Outline each P. falciparum parasite and classify it by life-cycle stage.
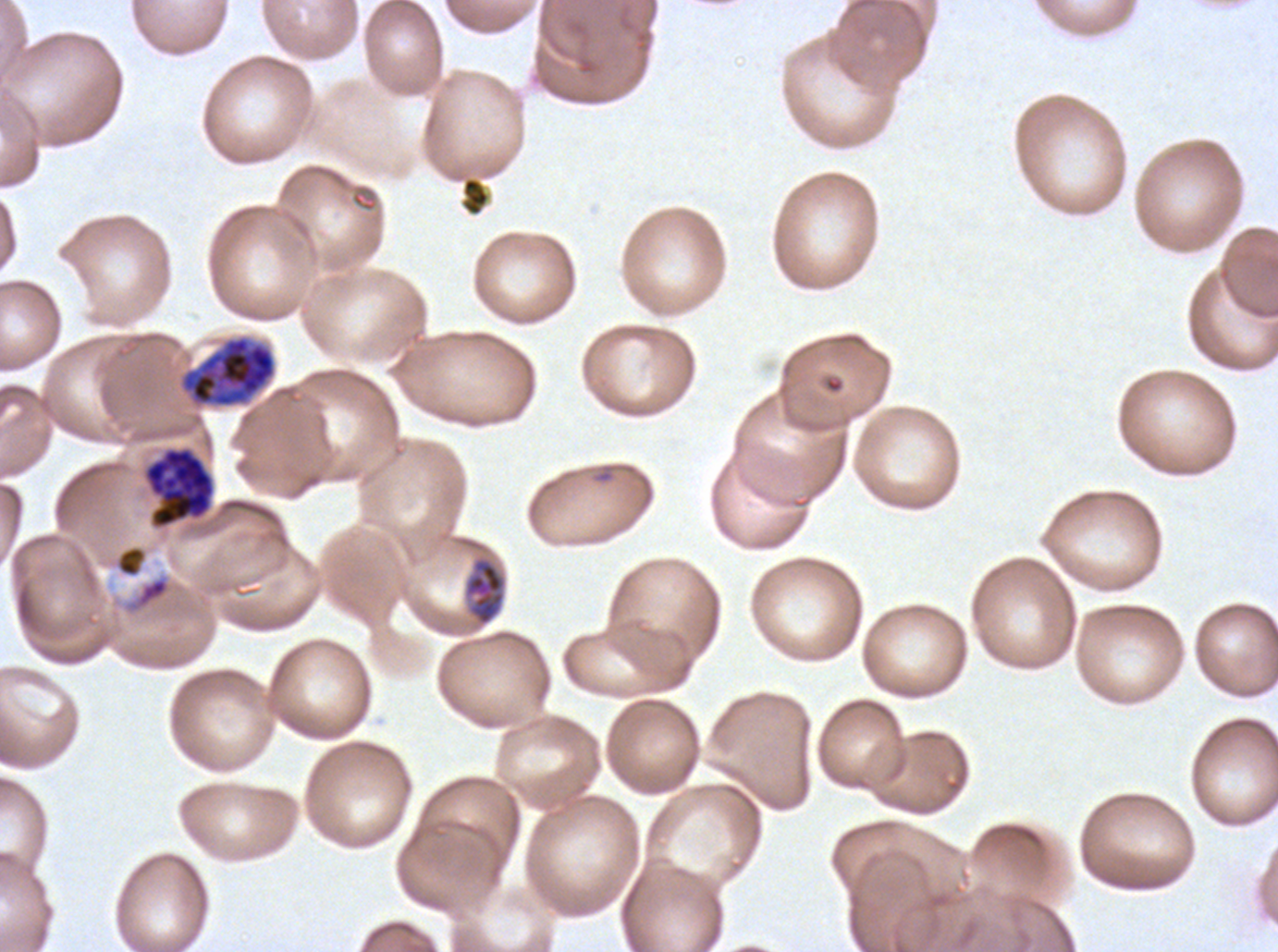

Approximate bounding boxes as {x1, y1, x2, y2} in pixels.
Mid trophozoites: {104, 543, 150, 580}, {463, 556, 506, 627}.
Early schizonts: {179, 336, 276, 408}.
Late schizonts: {143, 447, 215, 528}.
No rings, late-ring/early-trophozoite forms, late trophozoites, segmenters, or gametocytes observed.

image_size: 1278×952 pixels
preparation: thin blood film
debris_locations: 'approximate bounding boxes as {x1, y1, x2, y2} in pixels: {460, 176, 490, 216}'
stain: Giemsa
specimen: P. falciparum cultured ex vivo for 24 to 48 hours, from a patient in The Gambia
life_cycle_stages_observed: mid trophozoite, early schizont, late schizont
field_of_view: sub-image separated from a larger composite